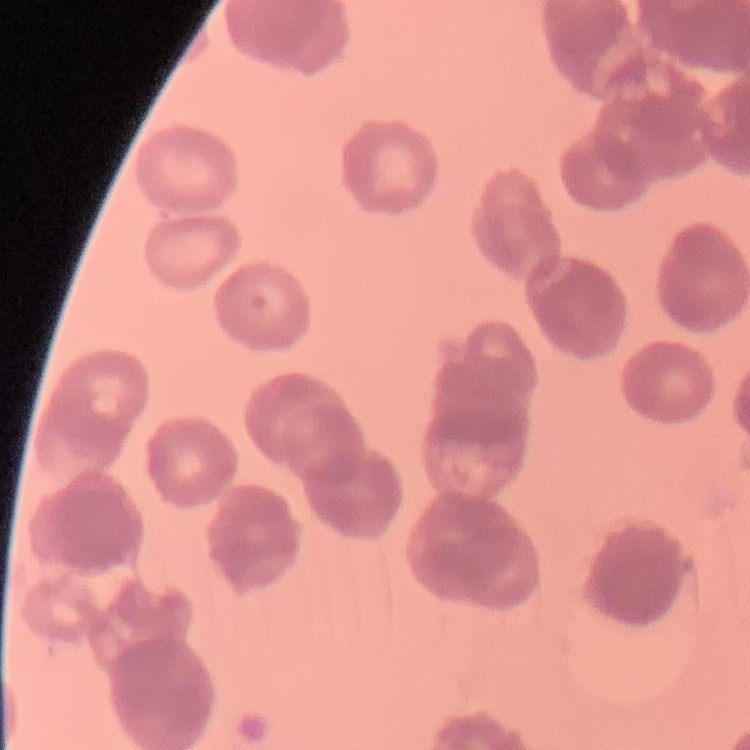 The erythrocytes exhibit rouleaux formation. Square crop of a larger photomicrograph. Field's or Giemsa stain. Thin blood smear.